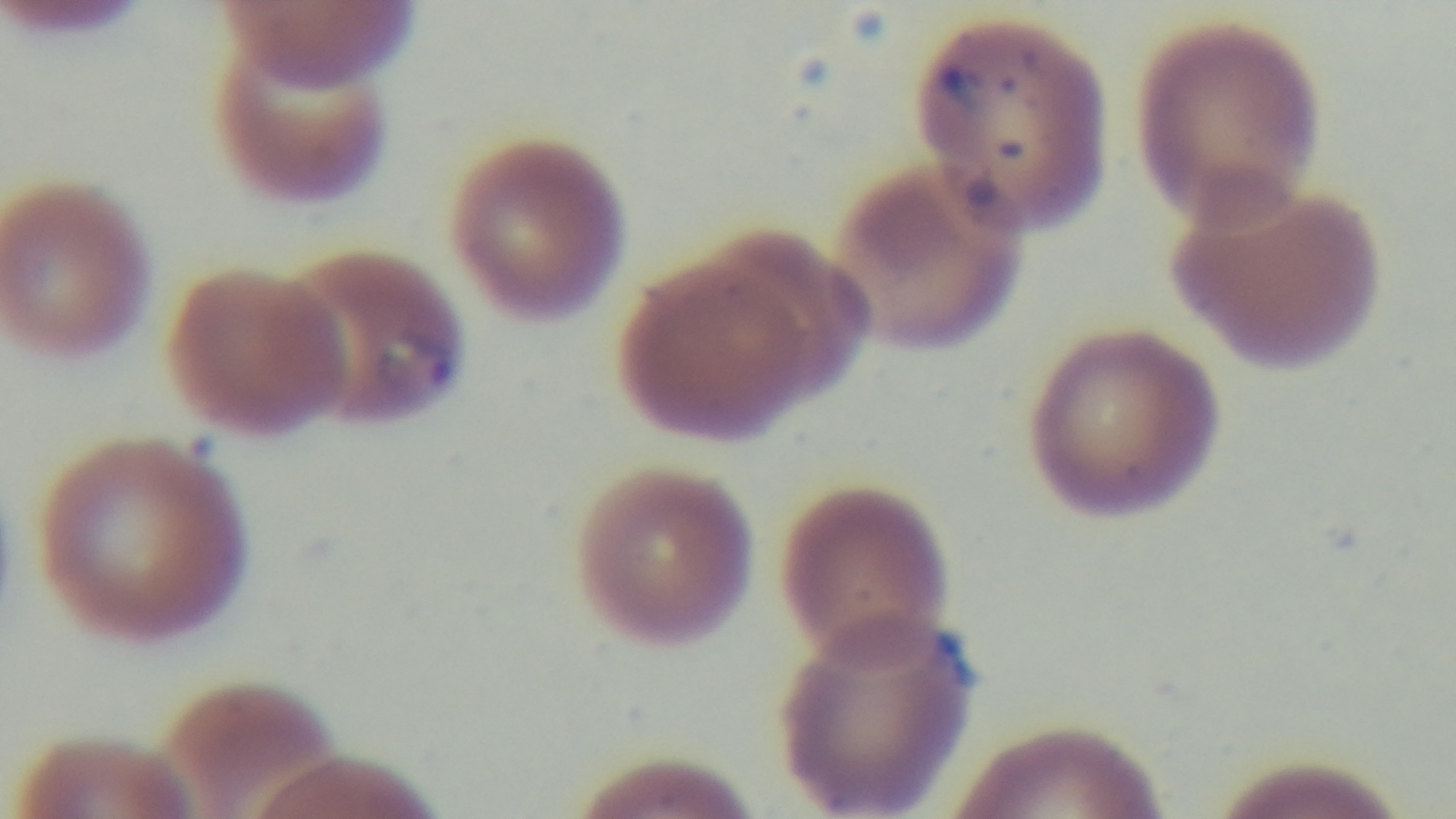

field of view = one from the slide
modality = light microscopy
stain = Giemsa
capture = mounted 4K digital camera
preparation = thin blood film
objective = 100x oil immersion
malaria status = infected